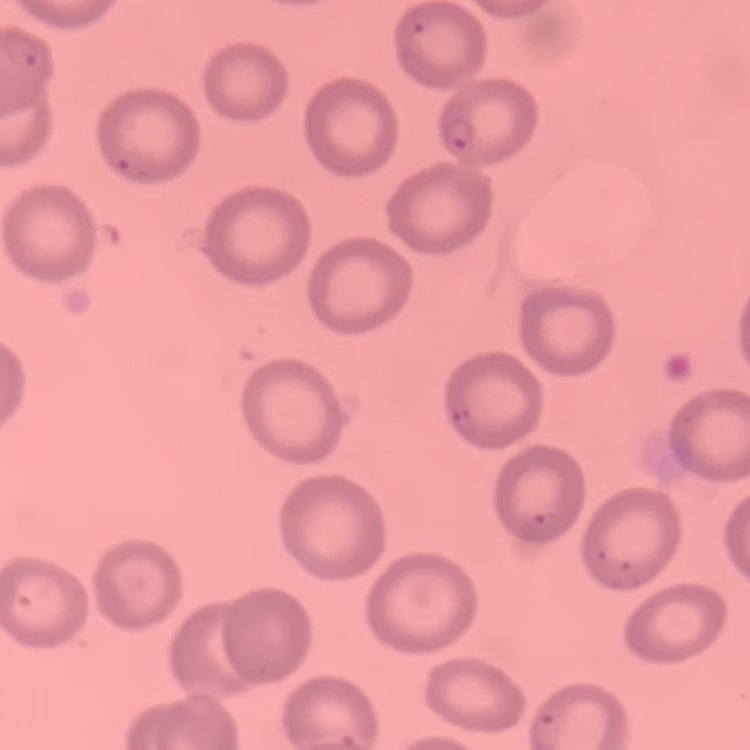

erythrocyte morphology = no rouleaux formation
stain = Field's or Giemsa
image type = one tile cut from a larger photomicrograph
preparation = thin blood film